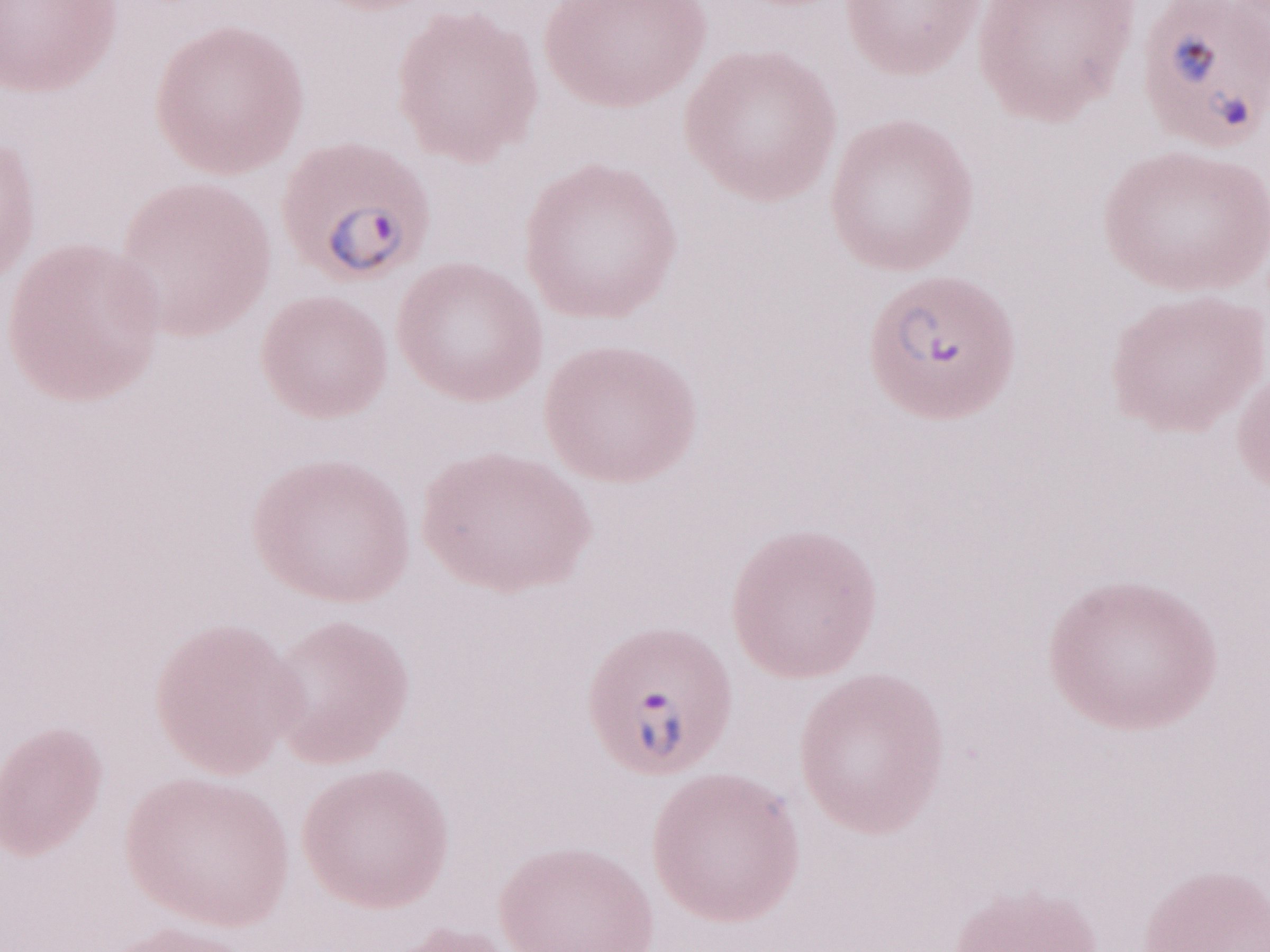
1,000x magnification. May-Grünwald-Giemsa-stained preparation. Olympus BX43 microscope, Olympus DP73 camera. Single field of view. Thin blood film. Image is 1270×952 pixels. Malaria diagnosis (patient-level): positive.